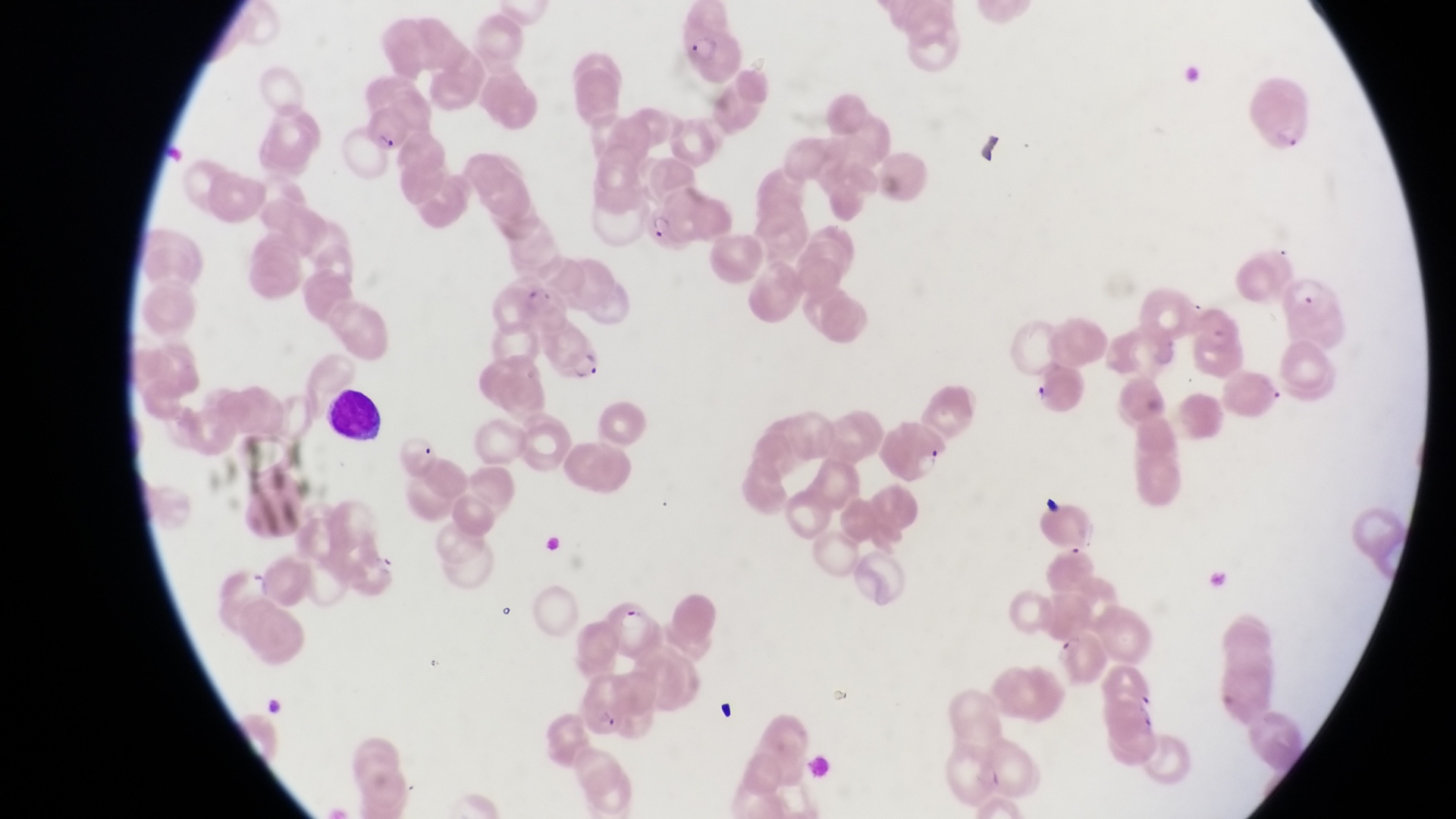
Approximate bounding boxes as [left, top, right, bottom] in pixels.
Summary:
  - Leukocyte locations: [327, 384, 385, 444]
  - Parasitised red blood cell locations: [680, 8, 752, 81], [1248, 73, 1317, 152], [642, 195, 709, 256], [1277, 270, 1344, 343], [549, 328, 608, 384], [888, 426, 948, 485], [394, 429, 440, 479], [602, 597, 661, 649], [576, 673, 639, 739]
  - Country: Uganda
  - Image size: 1456×819 pixels
  - Preparation: thin blood film
  - Capture: smartphone photograph through the eyepiece of an Olympus CX-23 microscope
  - Field of view: single
  - Magnification: 1000x